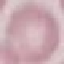

malaria status = uninfected
preparation = thin blood film
image type = automatically extracted cell patch, resized to 64 × 64 pixels
capture = smartphone through the microscope eyepiece
stain = Giemsa